Assess this cell for malaria.
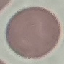

Uninfected.

image type = automatically extracted cell patch, resized to 64 × 64 pixels
capture = smartphone through the microscope eyepiece
stain = Giemsa
preparation = thin blood smear